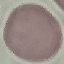 Malaria status: uninfected. Thin blood smear. Giemsa stain. Automatically extracted cell patch, resized to 64 × 64 pixels. Acquired by smartphone through the microscope eyepiece.